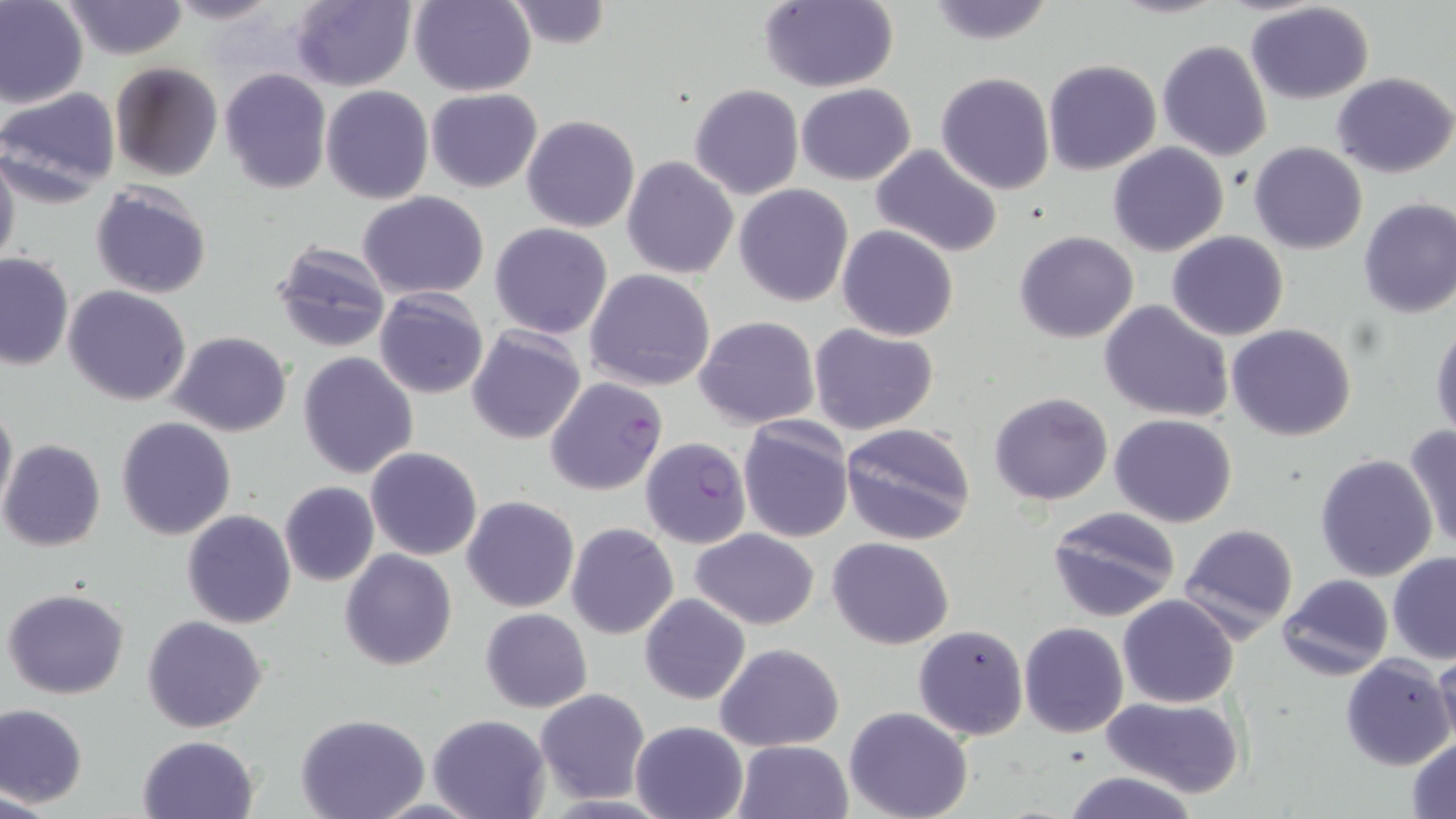

Approximate bounding boxes as named x1/y1/x2/y2 corners in pixels. Uninfected red blood cell locations: (x1=0, y1=0, x2=89, y2=109), (x1=61, y1=0, x2=187, y2=59), (x1=166, y1=0, x2=282, y2=24), (x1=288, y1=0, x2=417, y2=92), (x1=408, y1=0, x2=536, y2=96), (x1=503, y1=0, x2=611, y2=49), (x1=757, y1=1, x2=899, y2=92), (x1=922, y1=1, x2=1059, y2=47), (x1=1245, y1=2, x2=1377, y2=105), (x1=1156, y1=40, x2=1272, y2=163), (x1=1043, y1=59, x2=1162, y2=175), (x1=110, y1=62, x2=222, y2=181), (x1=219, y1=68, x2=333, y2=194), (x1=1332, y1=71, x2=1455, y2=178), (x1=935, y1=72, x2=1055, y2=193), (x1=797, y1=83, x2=915, y2=186), (x1=689, y1=84, x2=804, y2=200), (x1=321, y1=85, x2=434, y2=204), (x1=0, y1=86, x2=122, y2=205), (x1=426, y1=89, x2=543, y2=193), (x1=658, y1=108, x2=798, y2=249), (x1=506, y1=113, x2=624, y2=340), (x1=521, y1=115, x2=640, y2=233), (x1=1248, y1=142, x2=1367, y2=254), (x1=1108, y1=143, x2=1229, y2=257), (x1=869, y1=144, x2=1004, y2=258), (x1=0, y1=149, x2=20, y2=269), (x1=622, y1=156, x2=739, y2=279), (x1=89, y1=183, x2=213, y2=299), (x1=735, y1=183, x2=853, y2=305), (x1=358, y1=192, x2=490, y2=300), (x1=1357, y1=196, x2=1456, y2=318), (x1=490, y1=223, x2=613, y2=338), (x1=837, y1=225, x2=959, y2=342), (x1=1014, y1=231, x2=1139, y2=344), (x1=1168, y1=231, x2=1289, y2=341), (x1=270, y1=240, x2=394, y2=354), (x1=0, y1=253, x2=74, y2=371), (x1=584, y1=269, x2=715, y2=392), (x1=64, y1=285, x2=192, y2=405), (x1=374, y1=289, x2=489, y2=400), (x1=1101, y1=300, x2=1235, y2=423), (x1=694, y1=316, x2=820, y2=428), (x1=1429, y1=318, x2=1455, y2=442), (x1=809, y1=323, x2=940, y2=436), (x1=1228, y1=323, x2=1358, y2=441), (x1=465, y1=326, x2=588, y2=445), (x1=168, y1=330, x2=292, y2=436), (x1=297, y1=352, x2=419, y2=479), (x1=988, y1=391, x2=1114, y2=507), (x1=0, y1=397, x2=16, y2=522), (x1=1109, y1=413, x2=1238, y2=528), (x1=116, y1=416, x2=235, y2=540), (x1=738, y1=419, x2=853, y2=542), (x1=840, y1=422, x2=978, y2=545), (x1=1404, y1=426, x2=1456, y2=550), (x1=0, y1=439, x2=106, y2=552), (x1=365, y1=446, x2=483, y2=562), (x1=1314, y1=452, x2=1438, y2=582), (x1=279, y1=481, x2=380, y2=586), (x1=462, y1=495, x2=579, y2=612), (x1=1046, y1=506, x2=1181, y2=620), (x1=181, y1=510, x2=298, y2=629), (x1=567, y1=521, x2=678, y2=639), (x1=1181, y1=522, x2=1299, y2=644), (x1=692, y1=529, x2=819, y2=630), (x1=828, y1=537, x2=955, y2=649), (x1=339, y1=549, x2=458, y2=670), (x1=1388, y1=551, x2=1456, y2=664), (x1=1278, y1=573, x2=1394, y2=681), (x1=4, y1=587, x2=130, y2=698), (x1=1119, y1=593, x2=1238, y2=708), (x1=640, y1=594, x2=750, y2=705), (x1=480, y1=608, x2=592, y2=713), (x1=143, y1=614, x2=268, y2=733), (x1=1019, y1=621, x2=1129, y2=738), (x1=914, y1=624, x2=1028, y2=740), (x1=715, y1=643, x2=844, y2=751), (x1=1430, y1=649, x2=1456, y2=754), (x1=1339, y1=654, x2=1454, y2=771), (x1=535, y1=689, x2=650, y2=802), (x1=1102, y1=697, x2=1246, y2=800), (x1=0, y1=702, x2=88, y2=809), (x1=844, y1=707, x2=974, y2=819), (x1=296, y1=714, x2=430, y2=819), (x1=427, y1=714, x2=549, y2=819), (x1=629, y1=720, x2=748, y2=819), (x1=138, y1=734, x2=258, y2=818), (x1=1406, y1=736, x2=1456, y2=817), (x1=733, y1=740, x2=852, y2=818), (x1=1061, y1=770, x2=1202, y2=819). Plasmodium falciparum-infected red blood cell locations: (x1=544, y1=375, x2=667, y2=497), (x1=640, y1=436, x2=751, y2=548). Slide-level diagnosis: Plasmodium falciparum. May-Grünwald-Giemsa stain. Thin blood film. 1000x magnification. Optical microscopy. Image is 1456×819 pixels. Single field of view.